Draw a bounding box around every leukocyte (white blood cell).
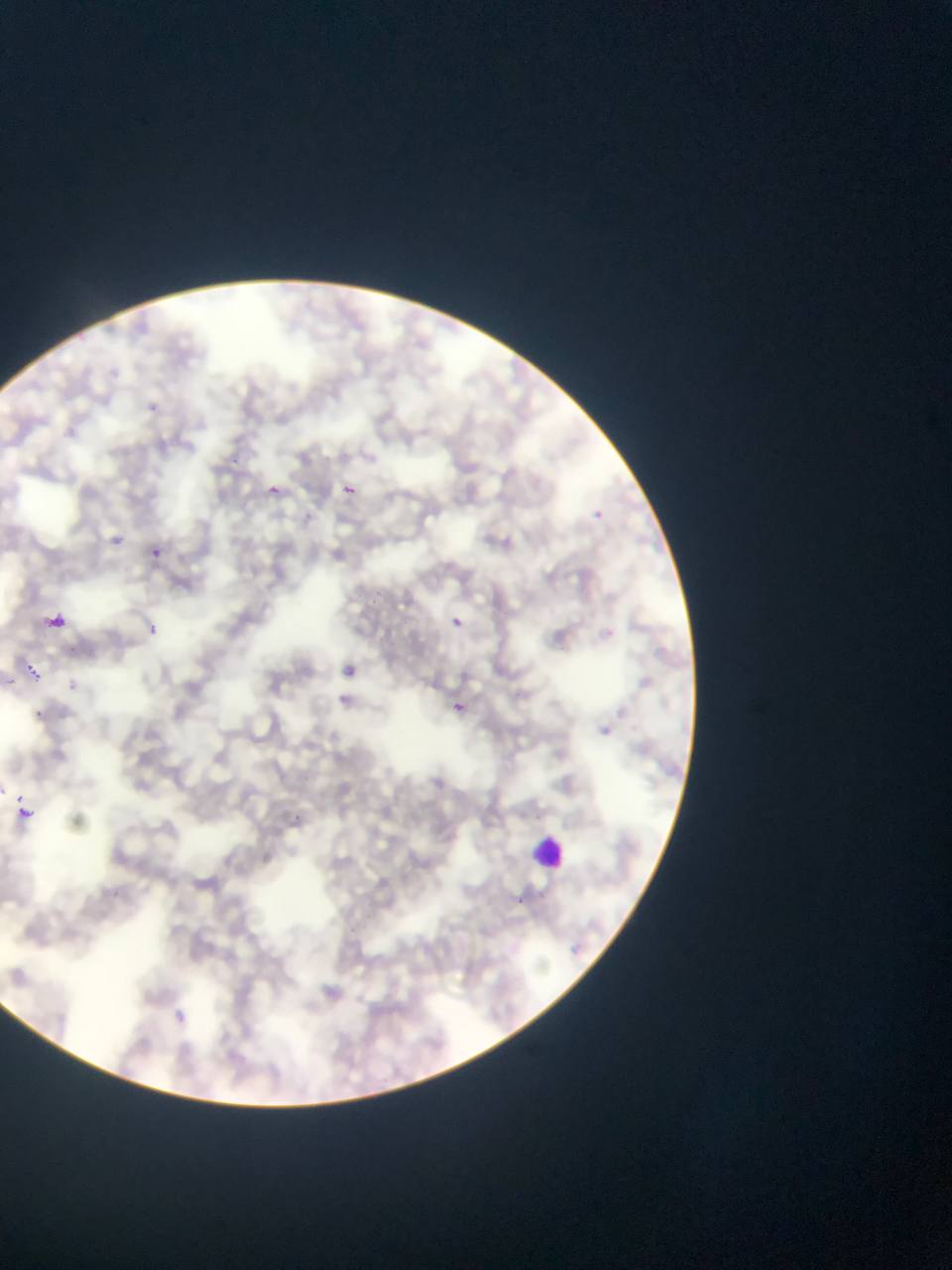
Approximate bounding boxes as (left, top, right, bottom) in pixels.
Leukocytes: (513, 812, 600, 877).

Malaria parasite locations: (145, 397, 164, 408), (272, 480, 287, 500), (341, 483, 359, 497), (596, 507, 613, 528), (109, 530, 134, 550), (150, 545, 166, 560), (443, 609, 469, 624), (46, 611, 69, 630), (141, 618, 168, 642), (19, 654, 43, 681), (453, 701, 467, 715), (28, 705, 53, 721), (15, 792, 26, 802), (17, 805, 33, 820). One field of view. Photographed through a microscope with a mobile-phone camera. Collected in Ghana. Thin blood film. Image is 952×1270 pixels.